Assess this cell for malaria.
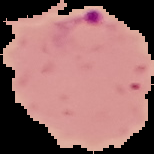
Parasitized.

From a thin blood smear. Segmented cell region on a black background. Image is 154×154 pixels.